Assess this cell for malaria.
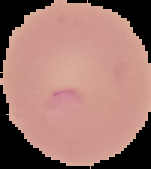

Uninfected.

Segmented cell region on a black background. From a thin blood film. Image is 151×169 pixels.